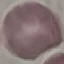
Summary:
  - Result: no malaria parasites seen
  - Preparation: thin blood film
  - Stain: Giemsa
  - Capture: smartphone camera at the microscope eyepiece
  - Image type: automatically extracted cell patch, resized to 64 × 64 pixels